Classify this cell by malaria status.
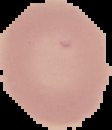

It is uninfected.

Cell region segmented out of the field of view; the surrounding area is masked to black. Image is 112×130 pixels. From a thin blood film.